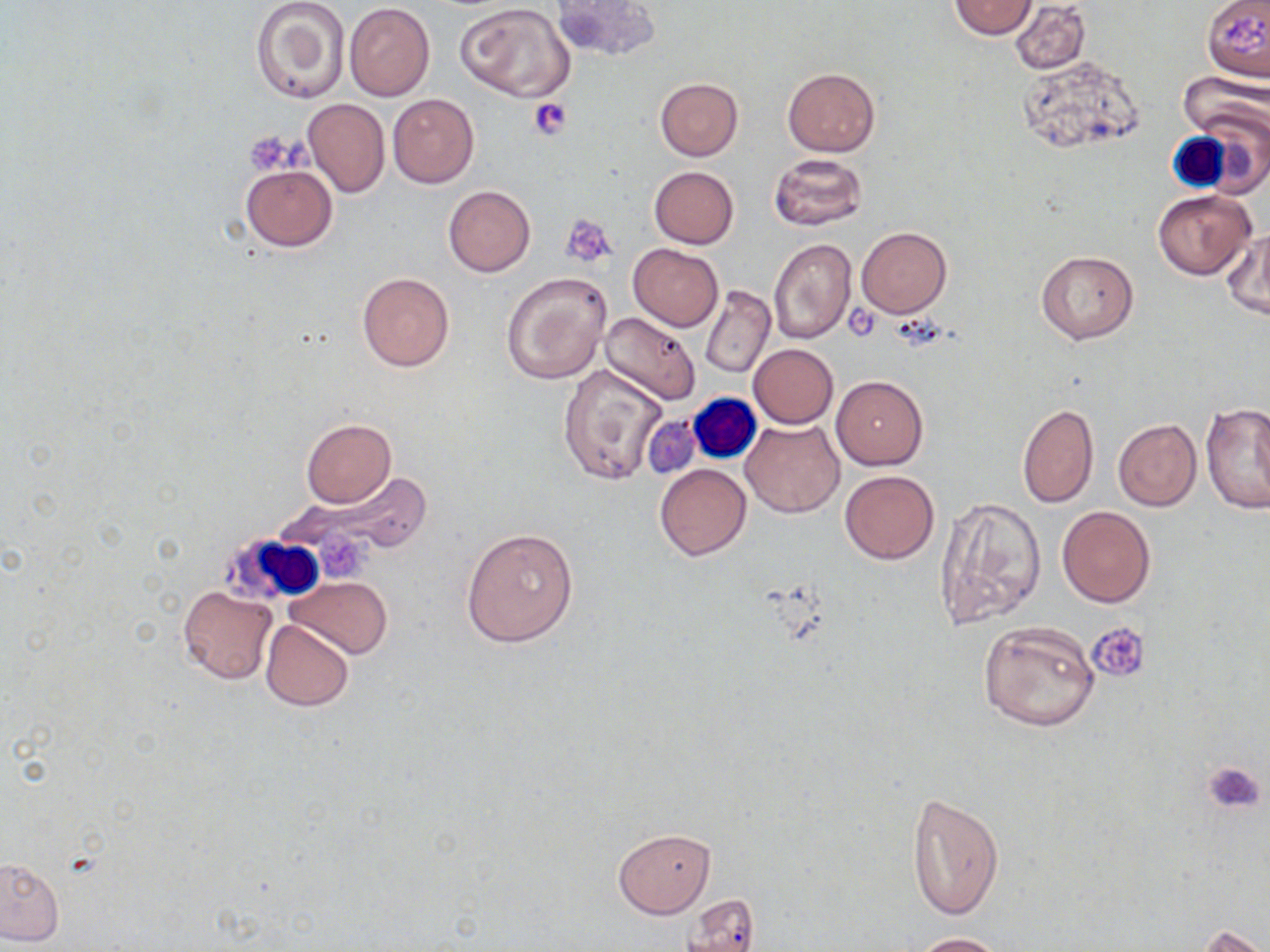
Approximate bounding boxes as named x1/y1/x2/y2 corners in pixels. Uninfected red blood cell locations: (x1=251, y1=0, x2=351, y2=104), (x1=553, y1=0, x2=661, y2=62), (x1=1009, y1=0, x2=1091, y2=75), (x1=1201, y1=0, x2=1269, y2=84), (x1=949, y1=1, x2=1035, y2=38), (x1=457, y1=2, x2=575, y2=102), (x1=343, y1=5, x2=435, y2=100), (x1=1018, y1=54, x2=1145, y2=158), (x1=783, y1=66, x2=879, y2=156), (x1=1179, y1=74, x2=1268, y2=142), (x1=654, y1=78, x2=743, y2=160), (x1=387, y1=93, x2=479, y2=188), (x1=301, y1=98, x2=389, y2=198), (x1=768, y1=153, x2=868, y2=231), (x1=241, y1=164, x2=337, y2=250), (x1=649, y1=166, x2=739, y2=248), (x1=443, y1=185, x2=535, y2=277), (x1=1152, y1=189, x2=1255, y2=279), (x1=857, y1=227, x2=951, y2=317), (x1=1220, y1=230, x2=1270, y2=320), (x1=768, y1=238, x2=858, y2=344), (x1=628, y1=244, x2=723, y2=331), (x1=1034, y1=249, x2=1139, y2=344), (x1=501, y1=270, x2=611, y2=385), (x1=358, y1=272, x2=454, y2=372), (x1=700, y1=284, x2=774, y2=378), (x1=599, y1=311, x2=702, y2=407), (x1=749, y1=343, x2=838, y2=428), (x1=558, y1=363, x2=667, y2=487), (x1=830, y1=375, x2=928, y2=469), (x1=1201, y1=402, x2=1269, y2=515), (x1=1017, y1=403, x2=1099, y2=507), (x1=644, y1=417, x2=699, y2=478), (x1=300, y1=419, x2=396, y2=508), (x1=740, y1=419, x2=842, y2=518), (x1=1112, y1=419, x2=1201, y2=511), (x1=655, y1=463, x2=751, y2=560), (x1=272, y1=470, x2=434, y2=563), (x1=839, y1=470, x2=939, y2=564), (x1=935, y1=497, x2=1046, y2=629), (x1=1057, y1=506, x2=1155, y2=608), (x1=461, y1=527, x2=578, y2=647), (x1=286, y1=575, x2=393, y2=660), (x1=176, y1=585, x2=277, y2=684), (x1=260, y1=620, x2=352, y2=711), (x1=978, y1=620, x2=1099, y2=732), (x1=906, y1=792, x2=1003, y2=922), (x1=613, y1=828, x2=714, y2=918), (x1=0, y1=857, x2=64, y2=946), (x1=681, y1=894, x2=761, y2=951), (x1=1193, y1=925, x2=1267, y2=952), (x1=907, y1=931, x2=1013, y2=951). White blood cell locations: (x1=689, y1=396, x2=759, y2=461), (x1=217, y1=533, x2=321, y2=603). Platelet locations: (x1=1220, y1=15, x2=1266, y2=57), (x1=528, y1=97, x2=571, y2=141), (x1=244, y1=130, x2=297, y2=176), (x1=560, y1=214, x2=617, y2=268), (x1=842, y1=309, x2=883, y2=341), (x1=1086, y1=622, x2=1149, y2=683), (x1=1202, y1=761, x2=1266, y2=816). Slide-level diagnosis: negative for blood parasites. May-Grünwald-Giemsa stain. Thin blood film. One field of a larger specimen. Captured at 1000x magnification. Image is 1270×952 pixels. Optical microscopy.